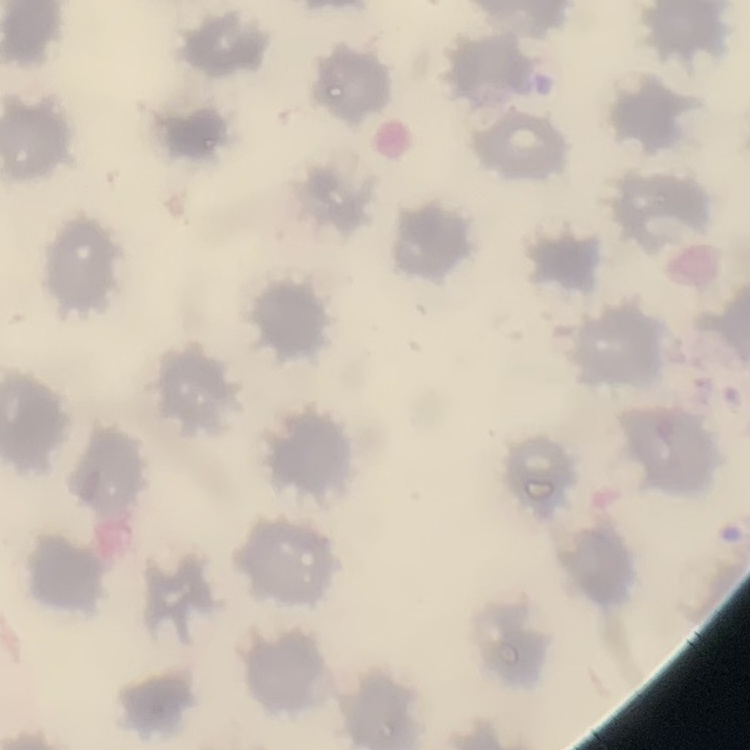

{
  "erythrocyte_morphology": "no rouleaux formation",
  "stain": "Field's or Giemsa",
  "preparation": "thin peripheral smear",
  "image_type": "one tile cut from a larger photomicrograph"
}